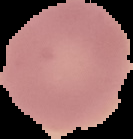

From a thin blood smear. Result: no Plasmodium parasites seen. Image is 133×139 pixels. The area outside the segmented cell region is set to black.